Give the position of every Plasmodium falciparum parasite, noting its life-cycle stage.
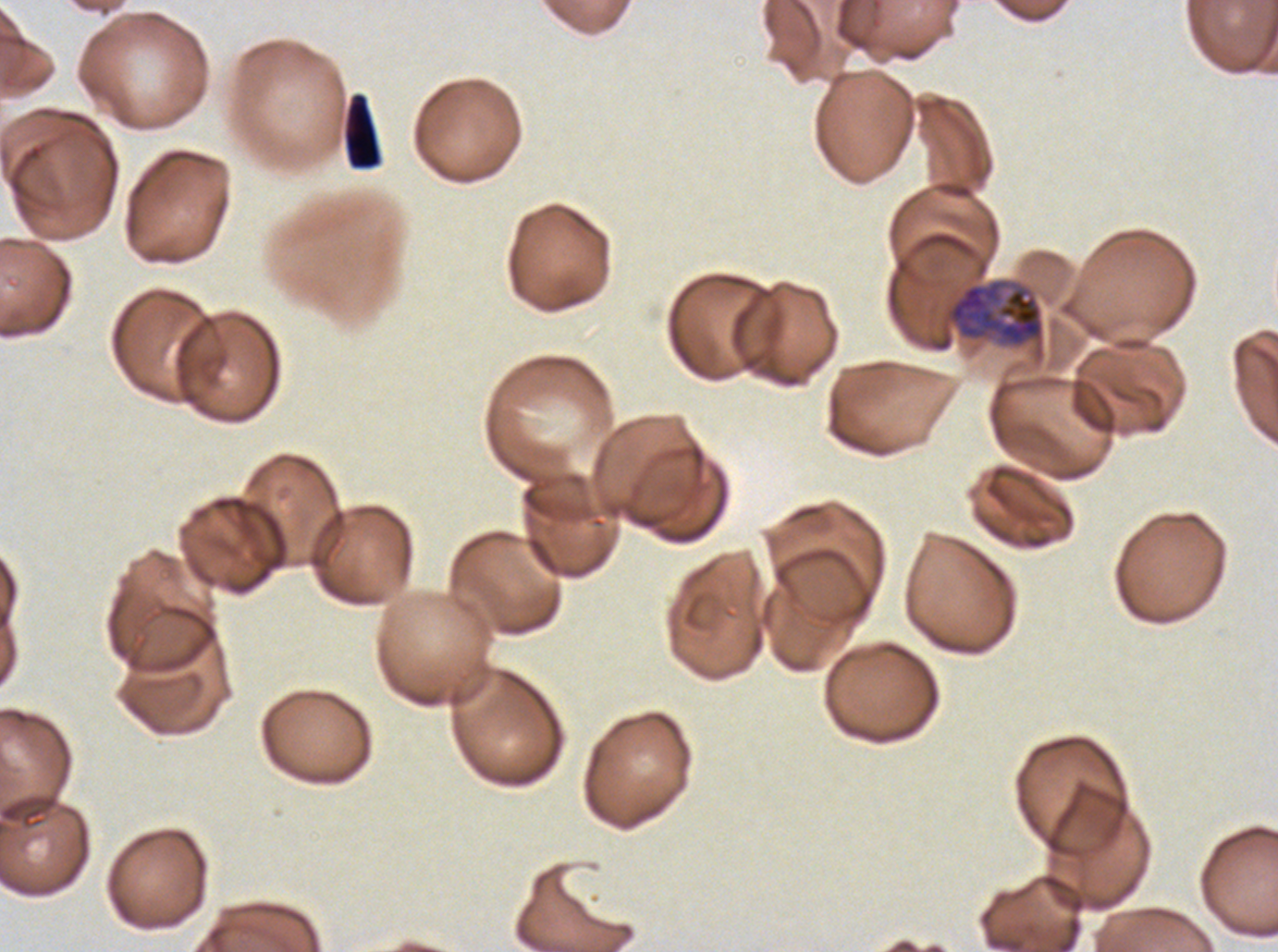
Approximate bounding boxes as [x1, y1, x2, y2] in pixels.
Early schizonts: [945, 279, 1045, 348].
No rings, late-ring/early-trophozoite forms, mid trophozoites, late trophozoites, late schizonts, segmenters, or gametocytes observed.

Debris locations: [342, 92, 382, 170]. Plasmodium falciparum cultured ex vivo for 24 to 48 hours, from a patient in The Gambia. Giemsa-stained preparation. Image is 1278×952 pixels. A sub-image separated from a larger composite. Thin blood smear.